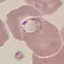

Malaria status: parasitized. Giemsa stain. Thin smear of blood. Cell patch, automatically extracted from a larger field of view and resized to 64 × 64 pixels. Acquired by smartphone through the microscope eyepiece.